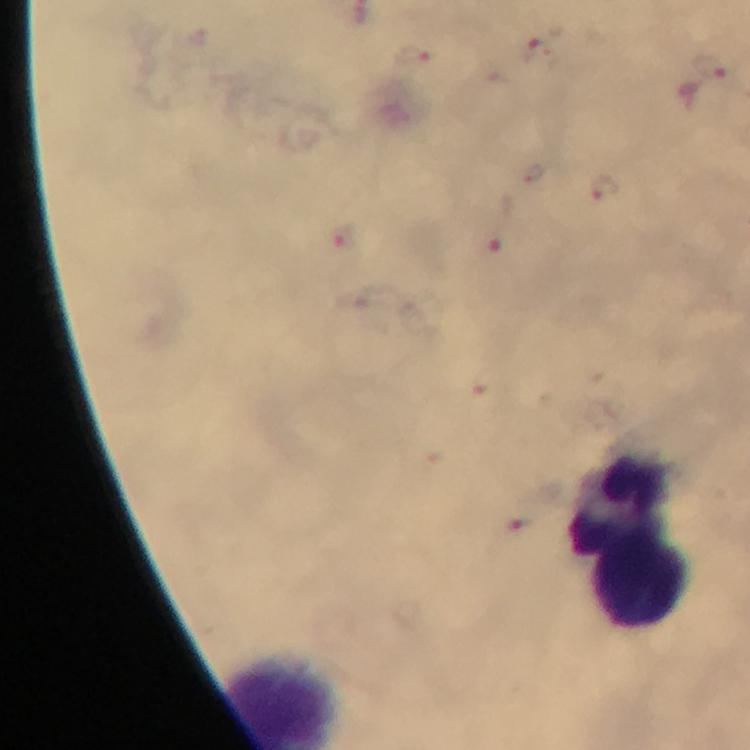

image size = 750×750 pixels
Plasmodium parasite locations = approximate centers as (x, y) in pixels: (536, 52), (414, 58), (710, 68), (606, 188), (343, 238), (491, 244)
immersion oil = applied
preparation = thick blood smear
leukocyte locations = approximate centers as (x, y) in pixels: (622, 497), (639, 584)
magnification = 100x
capture = smartphone photograph through a microscope
context = from a diagnostic examination for malaria
cropped from = one field of view
stain = Giemsa